Classify this cell by malaria status.
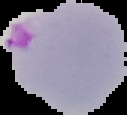

It is parasitized.

Segmented cell region on a black background. From a thin blood film. Image is 127×115 pixels.